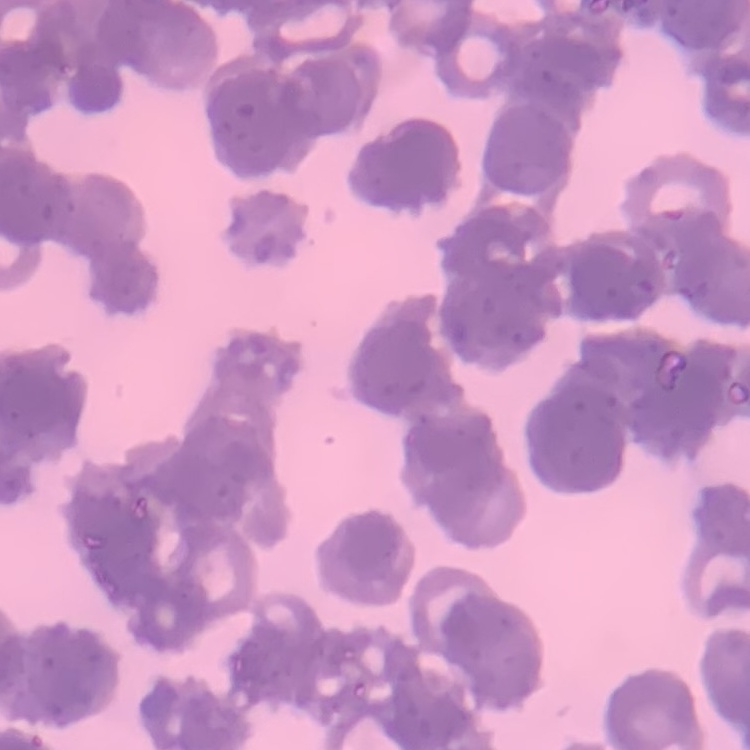
The erythrocytes exhibit rouleaux formation. Thin blood smear. Field's or Giemsa stain. One tile cut from a larger photomicrograph.